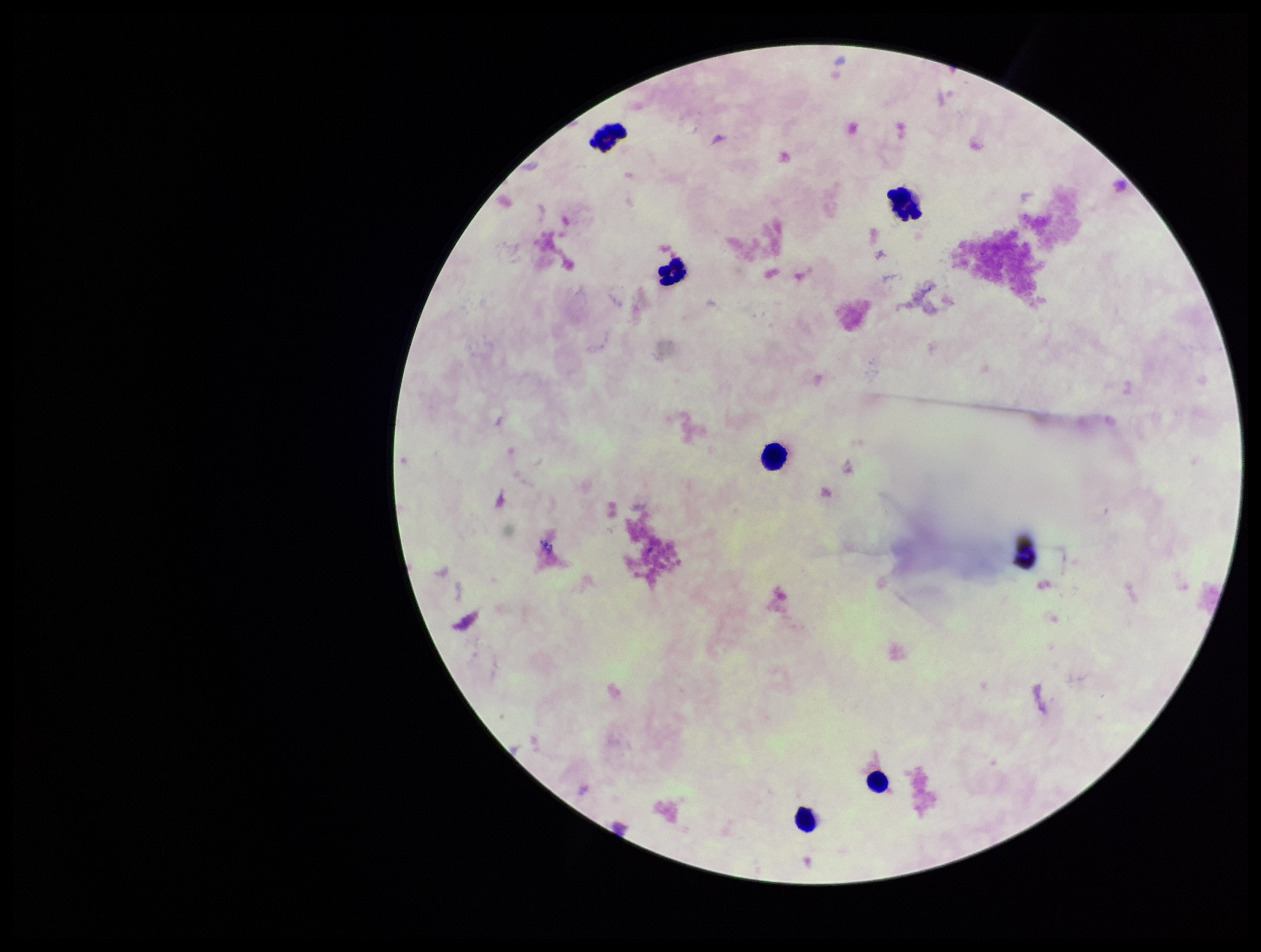

Summary:
  - Patient malaria status: negative
  - Stain: Giemsa
  - Plasmodium parasites: none seen
  - Leukocyte count: 6
  - Image size: 1261×952 pixels
  - Capture: smartphone photograph through the microscope eyepiece
  - Field of view: one from this slide
  - Parasite count: 0
  - Preparation: thick smear